Assess this cell for malaria.
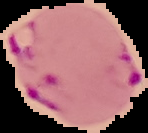

Parasitized.

preparation = thin blood film
image size = 148×133 pixels
image type = segmented cell region with the area outside set to black